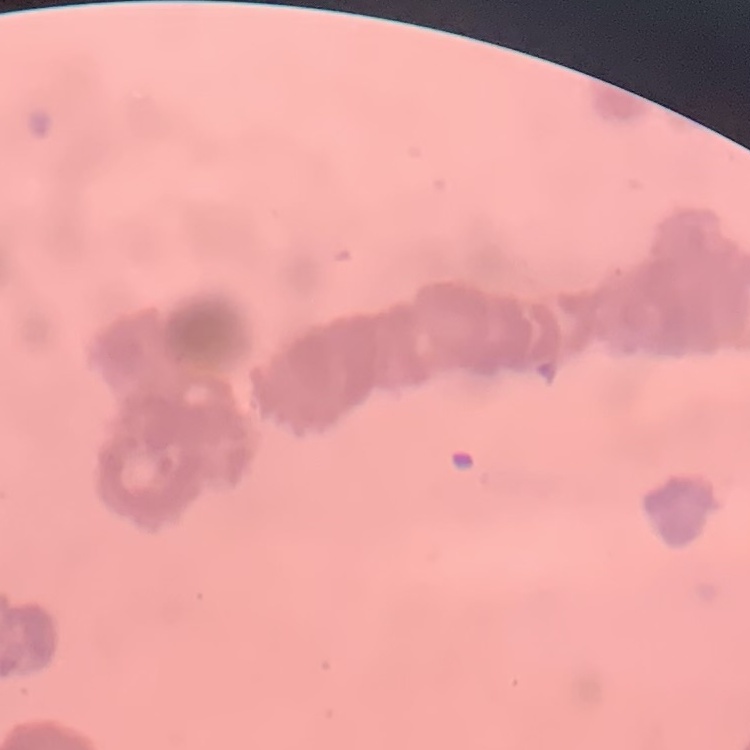

red blood cell morphology = rouleaux formation
preparation = thin blood film
stain = Field's or Giemsa
image type = one tile cut from a larger photomicrograph